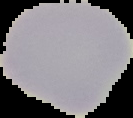
Summary:
  - Malaria status: uninfected
  - Preparation: thin blood film
  - Image size: 133×118 pixels
  - Image type: segmented cell region with the area outside set to black